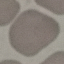 Malaria status: uninfected. Acquired by smartphone through the microscope eyepiece. Cell patch, automatically extracted from a larger field of view and resized to 64 × 64 pixels. Thin smear of blood. Giemsa-stained preparation.